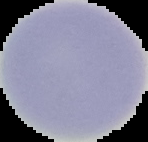 Segmented cell region on a black background. Result: negative for Plasmodium parasites. Image is 148×142 pixels. From a thin blood film.